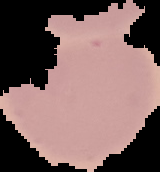
Result: no malaria parasites detected. Image is 160×172 pixels. From a thin blood smear. Segmented cell region on a black background.